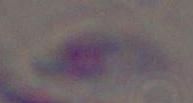
{
  "modality": "photomicrograph",
  "identification": "Toxoplasma gondii",
  "magnification": "1000x"
}